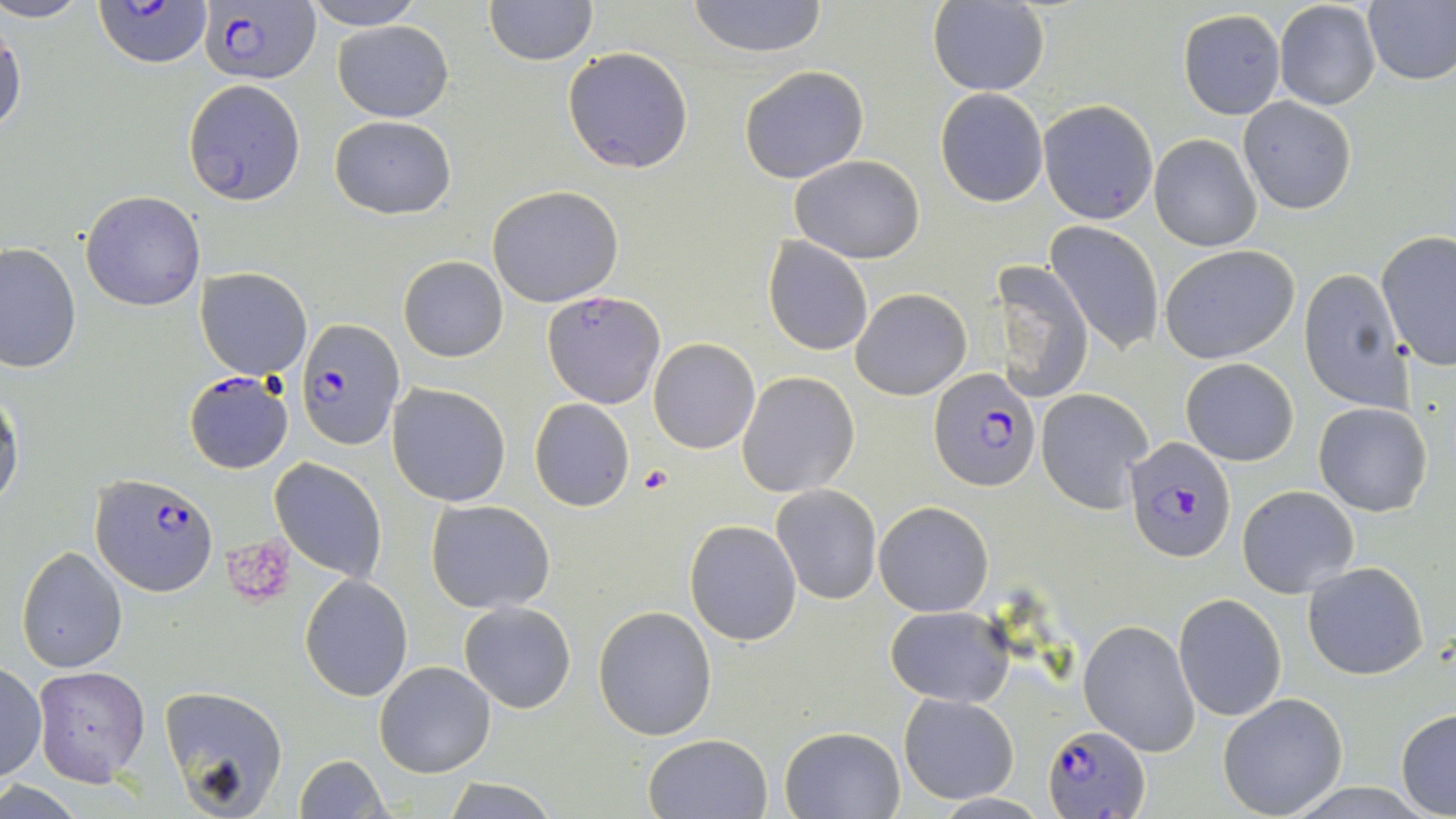
{
  "plasmodium_falciparum_infected_red_blood_cell_locations": "approximate bounding boxes as named x1/y1/x2/y2 corners in pixels: (x1=96, y1=1, x2=213, y2=68), (x1=201, y1=1, x2=321, y2=85), (x1=544, y1=289, x2=664, y2=408), (x1=296, y1=318, x2=403, y2=450), (x1=927, y1=367, x2=1042, y2=493), (x1=183, y1=370, x2=294, y2=473), (x1=1123, y1=436, x2=1235, y2=563), (x1=89, y1=473, x2=217, y2=596), (x1=1045, y1=724, x2=1154, y2=816)",
  "slide_level_diagnosis": "Plasmodium falciparum",
  "field_of_view": "one of a larger specimen",
  "platelet_locations": "approximate bounding boxes as named x1/y1/x2/y2 corners in pixels: (x1=638, y1=463, x2=675, y2=495), (x1=221, y1=538, x2=298, y2=610)",
  "uninfected_red_blood_cell_locations": "approximate bounding boxes as named x1/y1/x2/y2 corners in pixels: (x1=0, y1=0, x2=95, y2=24), (x1=300, y1=0, x2=426, y2=29), (x1=484, y1=0, x2=597, y2=66), (x1=686, y1=0, x2=828, y2=59), (x1=1273, y1=0, x2=1382, y2=111), (x1=1362, y1=0, x2=1456, y2=87), (x1=929, y1=2, x2=1050, y2=96), (x1=1178, y1=9, x2=1287, y2=120), (x1=0, y1=13, x2=26, y2=144), (x1=332, y1=19, x2=454, y2=122), (x1=562, y1=46, x2=694, y2=173), (x1=738, y1=65, x2=870, y2=183), (x1=182, y1=79, x2=306, y2=205), (x1=935, y1=87, x2=1048, y2=207), (x1=1238, y1=97, x2=1356, y2=213), (x1=1038, y1=99, x2=1158, y2=225), (x1=328, y1=114, x2=457, y2=220), (x1=1150, y1=134, x2=1262, y2=252), (x1=791, y1=155, x2=925, y2=264), (x1=81, y1=190, x2=206, y2=311), (x1=488, y1=192, x2=626, y2=314), (x1=1045, y1=220, x2=1166, y2=355), (x1=1377, y1=231, x2=1456, y2=370), (x1=763, y1=238, x2=873, y2=356), (x1=0, y1=242, x2=80, y2=375), (x1=1159, y1=244, x2=1300, y2=364), (x1=398, y1=255, x2=509, y2=362), (x1=995, y1=258, x2=1094, y2=405), (x1=194, y1=267, x2=312, y2=380), (x1=1298, y1=268, x2=1411, y2=412), (x1=850, y1=287, x2=972, y2=401), (x1=648, y1=338, x2=760, y2=453), (x1=1180, y1=357, x2=1300, y2=468), (x1=737, y1=370, x2=859, y2=498), (x1=387, y1=383, x2=511, y2=506), (x1=0, y1=387, x2=23, y2=515), (x1=1036, y1=388, x2=1153, y2=514), (x1=529, y1=398, x2=635, y2=512), (x1=1313, y1=401, x2=1435, y2=518), (x1=270, y1=458, x2=387, y2=582), (x1=771, y1=484, x2=882, y2=604), (x1=1237, y1=484, x2=1359, y2=598), (x1=426, y1=499, x2=555, y2=612), (x1=874, y1=501, x2=995, y2=617), (x1=684, y1=520, x2=801, y2=645), (x1=16, y1=546, x2=129, y2=674), (x1=1303, y1=562, x2=1430, y2=679), (x1=300, y1=575, x2=414, y2=701), (x1=1173, y1=594, x2=1286, y2=721), (x1=459, y1=600, x2=576, y2=713), (x1=592, y1=604, x2=717, y2=740), (x1=886, y1=605, x2=1013, y2=708), (x1=1078, y1=618, x2=1199, y2=756), (x1=374, y1=661, x2=497, y2=778), (x1=0, y1=662, x2=46, y2=783), (x1=34, y1=667, x2=152, y2=787), (x1=159, y1=684, x2=291, y2=815), (x1=897, y1=692, x2=1018, y2=804), (x1=1217, y1=692, x2=1348, y2=816), (x1=1395, y1=708, x2=1456, y2=816), (x1=780, y1=726, x2=906, y2=819), (x1=645, y1=733, x2=772, y2=818), (x1=293, y1=753, x2=390, y2=819), (x1=443, y1=778, x2=558, y2=818)",
  "stain": "May-Grünwald-Giemsa",
  "image_size": "1456×819 pixels",
  "preparation": "thin blood film",
  "modality": "optical microscopy",
  "magnification": "1000x"
}